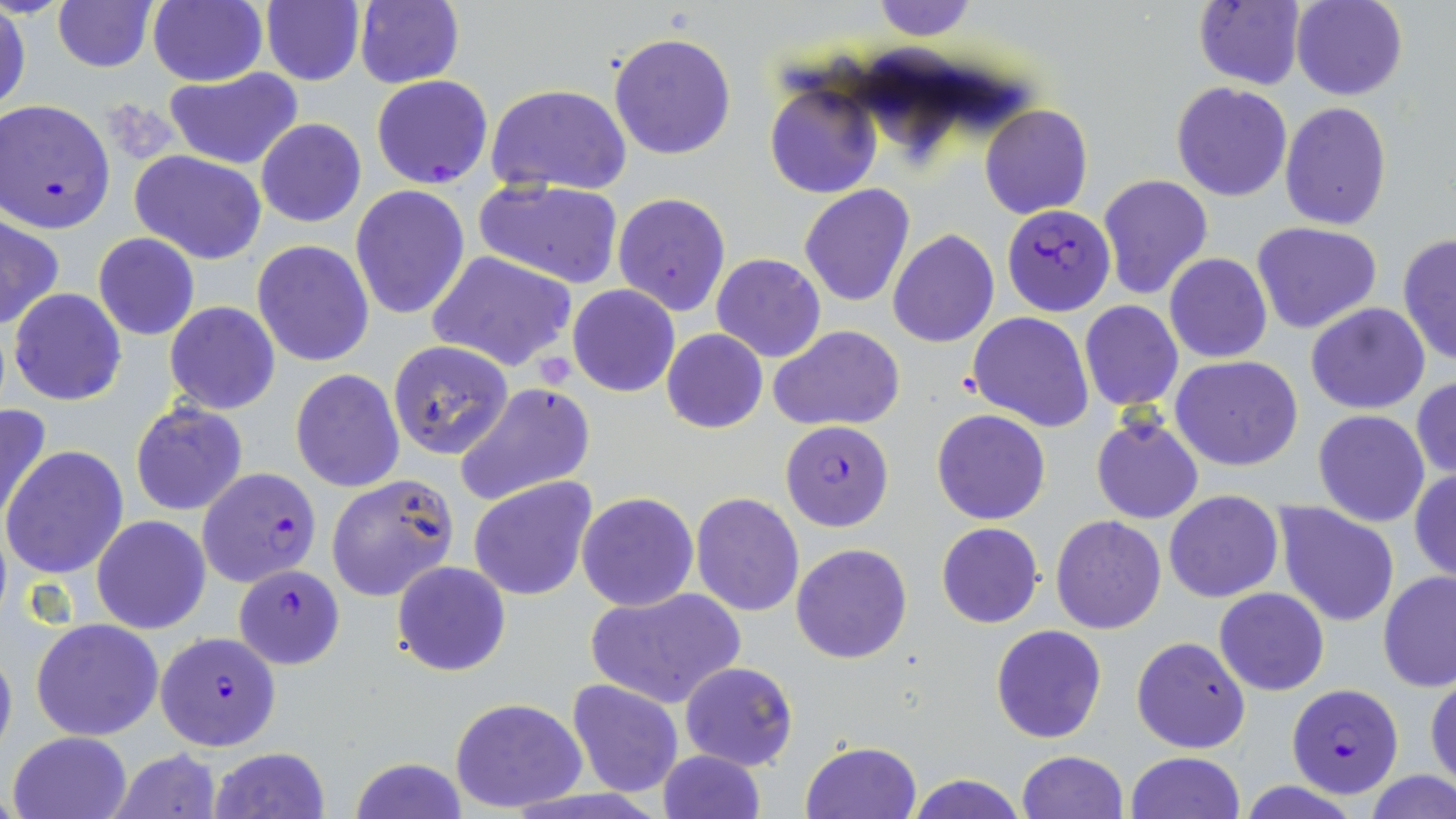 Approximate bounding boxes as named x1/y1/x2/y2 corners in pixels. Uninfected red blood cell locations: (x1=148, y1=0, x2=267, y2=86), (x1=260, y1=0, x2=365, y2=86), (x1=355, y1=0, x2=465, y2=90), (x1=868, y1=0, x2=978, y2=41), (x1=1293, y1=0, x2=1407, y2=101), (x1=52, y1=1, x2=157, y2=72), (x1=1192, y1=1, x2=1305, y2=89), (x1=1, y1=5, x2=30, y2=116), (x1=608, y1=30, x2=737, y2=160), (x1=163, y1=68, x2=305, y2=169), (x1=764, y1=81, x2=883, y2=200), (x1=1171, y1=82, x2=1294, y2=201), (x1=486, y1=83, x2=632, y2=196), (x1=1279, y1=102, x2=1392, y2=230), (x1=979, y1=103, x2=1093, y2=219), (x1=256, y1=118, x2=366, y2=229), (x1=130, y1=150, x2=267, y2=265), (x1=1097, y1=173, x2=1213, y2=299), (x1=474, y1=177, x2=625, y2=288), (x1=349, y1=184, x2=471, y2=321), (x1=798, y1=184, x2=916, y2=308), (x1=613, y1=192, x2=730, y2=317), (x1=1, y1=216, x2=63, y2=330), (x1=1253, y1=221, x2=1383, y2=333), (x1=888, y1=228, x2=999, y2=348), (x1=93, y1=233, x2=200, y2=341), (x1=1397, y1=233, x2=1456, y2=365), (x1=252, y1=239, x2=374, y2=366), (x1=427, y1=250, x2=576, y2=373), (x1=1164, y1=252, x2=1273, y2=363), (x1=711, y1=254, x2=827, y2=362), (x1=266, y1=255, x2=390, y2=467), (x1=568, y1=285, x2=680, y2=398), (x1=8, y1=288, x2=127, y2=406), (x1=1078, y1=300, x2=1183, y2=412), (x1=164, y1=301, x2=280, y2=414), (x1=1306, y1=302, x2=1431, y2=414), (x1=967, y1=312, x2=1094, y2=430), (x1=770, y1=325, x2=906, y2=432), (x1=661, y1=328, x2=768, y2=433), (x1=387, y1=341, x2=514, y2=460), (x1=1171, y1=355, x2=1304, y2=471), (x1=290, y1=369, x2=405, y2=492), (x1=1411, y1=375, x2=1456, y2=479), (x1=455, y1=382, x2=595, y2=506), (x1=129, y1=400, x2=249, y2=517), (x1=0, y1=402, x2=54, y2=531), (x1=932, y1=409, x2=1051, y2=525), (x1=1313, y1=409, x2=1431, y2=527), (x1=1090, y1=417, x2=1204, y2=523), (x1=3, y1=446, x2=130, y2=579), (x1=1410, y1=470, x2=1456, y2=582), (x1=325, y1=474, x2=460, y2=603), (x1=467, y1=476, x2=599, y2=603), (x1=1165, y1=490, x2=1284, y2=603), (x1=576, y1=493, x2=699, y2=612), (x1=690, y1=493, x2=805, y2=616), (x1=1274, y1=503, x2=1399, y2=626), (x1=91, y1=515, x2=210, y2=634), (x1=1051, y1=515, x2=1167, y2=634), (x1=936, y1=522, x2=1042, y2=628), (x1=791, y1=542, x2=912, y2=664), (x1=391, y1=560, x2=510, y2=677), (x1=1378, y1=571, x2=1456, y2=693), (x1=586, y1=586, x2=746, y2=709), (x1=1214, y1=587, x2=1329, y2=695), (x1=30, y1=618, x2=163, y2=739), (x1=991, y1=624, x2=1108, y2=744), (x1=1130, y1=634, x2=1251, y2=754), (x1=0, y1=638, x2=17, y2=763), (x1=678, y1=661, x2=799, y2=770), (x1=1426, y1=675, x2=1456, y2=789), (x1=567, y1=679, x2=686, y2=799), (x1=449, y1=696, x2=588, y2=811), (x1=8, y1=730, x2=133, y2=819), (x1=802, y1=741, x2=921, y2=818), (x1=208, y1=746, x2=330, y2=819), (x1=109, y1=749, x2=222, y2=819), (x1=658, y1=749, x2=766, y2=819), (x1=1015, y1=750, x2=1128, y2=819), (x1=1126, y1=751, x2=1245, y2=819), (x1=348, y1=757, x2=470, y2=818), (x1=1365, y1=769, x2=1456, y2=819), (x1=906, y1=773, x2=1028, y2=819). Plasmodium falciparum-infected red blood cell locations: (x1=371, y1=75, x2=493, y2=190), (x1=0, y1=98, x2=114, y2=231), (x1=1003, y1=204, x2=1115, y2=315), (x1=780, y1=420, x2=894, y2=531), (x1=196, y1=468, x2=322, y2=588), (x1=233, y1=563, x2=346, y2=669), (x1=155, y1=630, x2=282, y2=751), (x1=1287, y1=683, x2=1405, y2=798). Platelet locations: (x1=539, y1=355, x2=577, y2=388). Slide-level diagnosis: Plasmodium falciparum. May-Grünwald-Giemsa-stained preparation. One field of a larger specimen. 1000x magnification. Thin blood film. Image is 1456×819 pixels. Light microscopy.